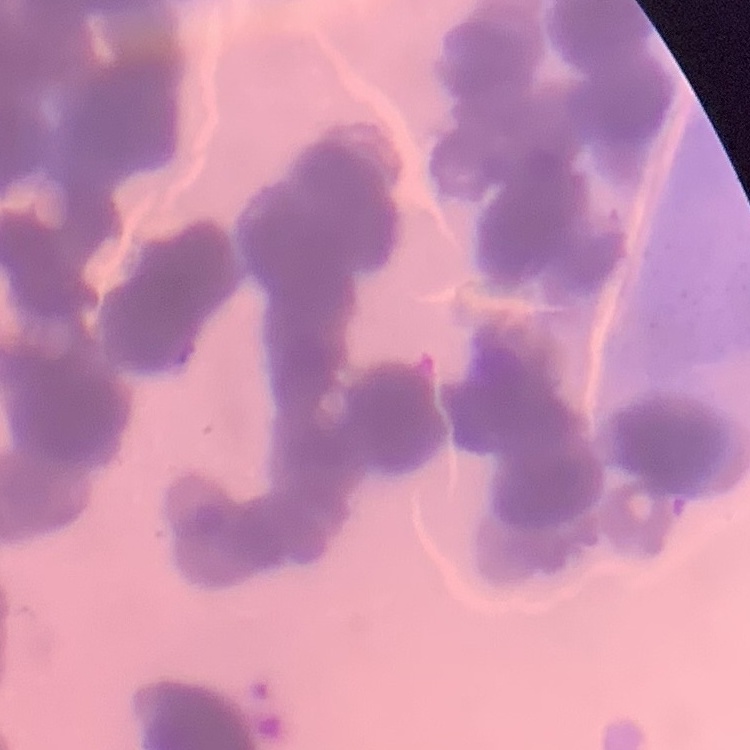

The erythrocytes exhibit rouleaux formation. Stained with either Field's or Giemsa. One tile cut from a larger photomicrograph. Thin blood film.